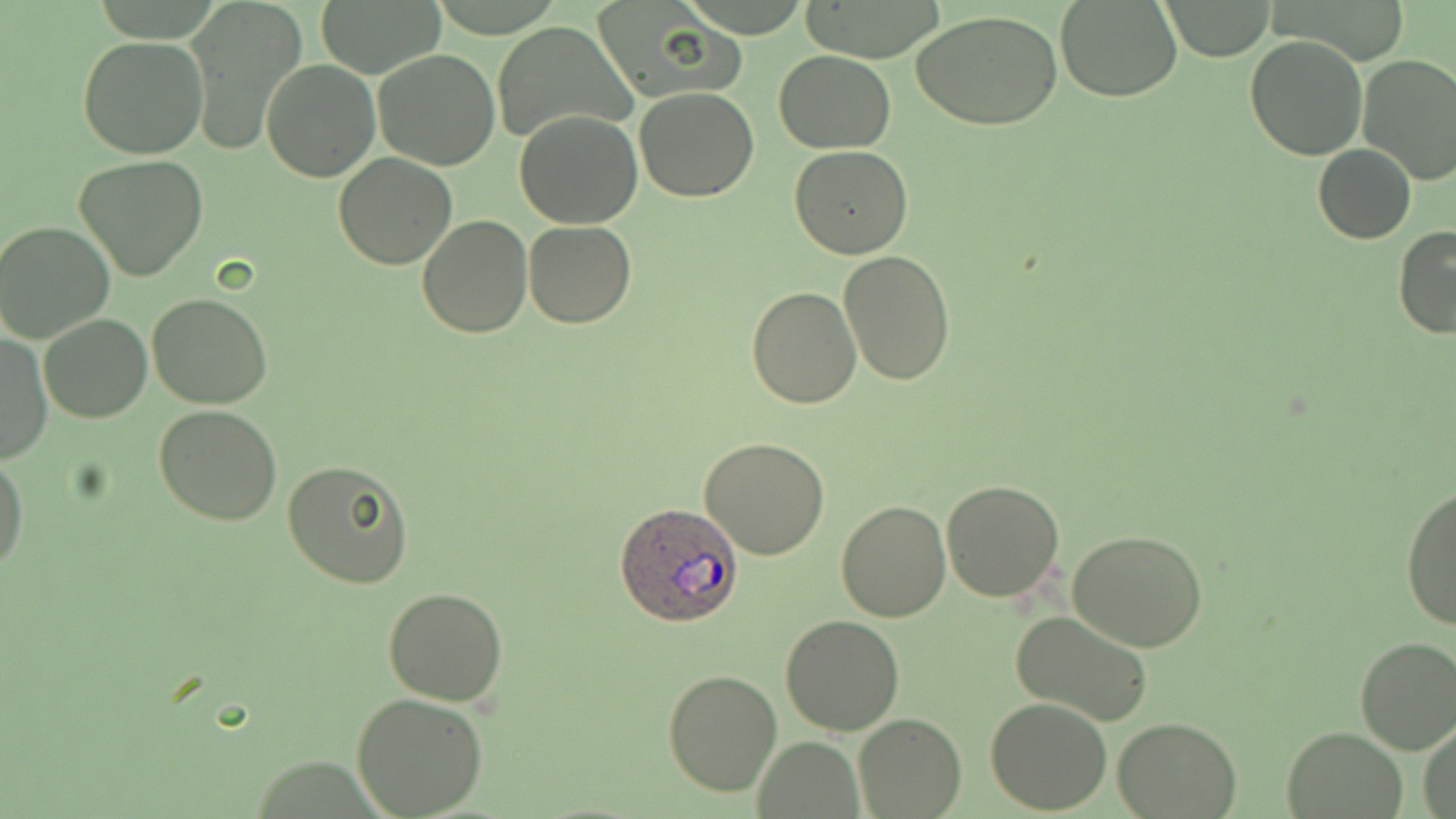
slide-level diagnosis = Plasmodium ovale
stain = May-Grünwald-Giemsa
field of view = one of a larger specimen
preparation = thin blood film
image size = 1456×819 pixels
Plasmodium ovale-infected red blood cell locations = approximate bounding boxes as (x1,y1)-(x2,y2) corner pairs in pixels: (618,504)-(744,625)
magnification = 1000x
uninfected red blood cell locations = approximate bounding boxes as (x1,y1)-(x2,y2) corner pairs in pixels: (181,0)-(308,156), (315,0)-(446,77), (1158,0)-(1276,60), (1055,1)-(1182,102), (589,3)-(745,106), (914,10)-(1064,131), (492,20)-(636,145), (1245,33)-(1367,158), (76,35)-(209,159), (372,49)-(501,170), (774,50)-(895,153), (1357,55)-(1456,185), (261,59)-(381,183), (634,86)-(760,202), (513,110)-(642,229), (790,145)-(912,258), (1313,145)-(1417,242), (333,154)-(458,270), (73,156)-(210,283), (418,214)-(532,338), (0,219)-(113,343), (523,220)-(636,328), (1393,225)-(1456,340), (839,250)-(956,386), (747,285)-(861,407), (148,292)-(274,408), (37,313)-(152,423), (0,331)-(51,463), (153,404)-(282,526), (698,436)-(831,559), (0,449)-(28,573), (282,459)-(413,589), (941,480)-(1066,602), (1400,484)-(1456,631), (835,499)-(953,622), (1066,529)-(1210,652), (383,588)-(509,705), (1010,610)-(1154,727), (779,615)-(906,736), (1354,636)-(1456,755), (662,667)-(782,796), (351,692)-(489,818), (985,698)-(1113,815), (854,714)-(965,818), (1114,716)-(1242,819), (1420,724)-(1456,819), (1281,726)-(1406,817), (754,737)-(865,818)
modality = light microscopy